Identify the parasite.
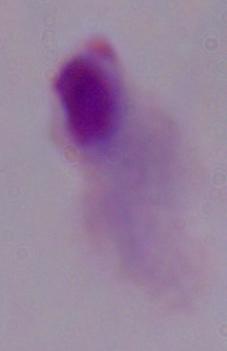
A trichomonad.

Captured at 1000x magnification. Photomicrograph.